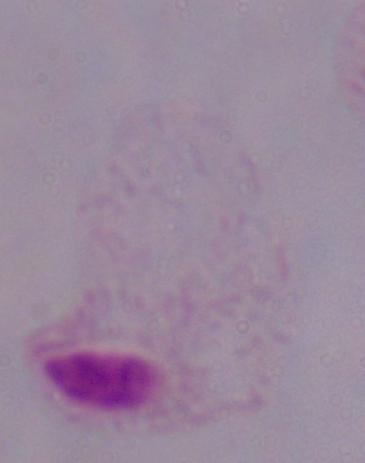
magnification = 1000x
identification = trichomonad
modality = micrograph